Name the blood parasite species.
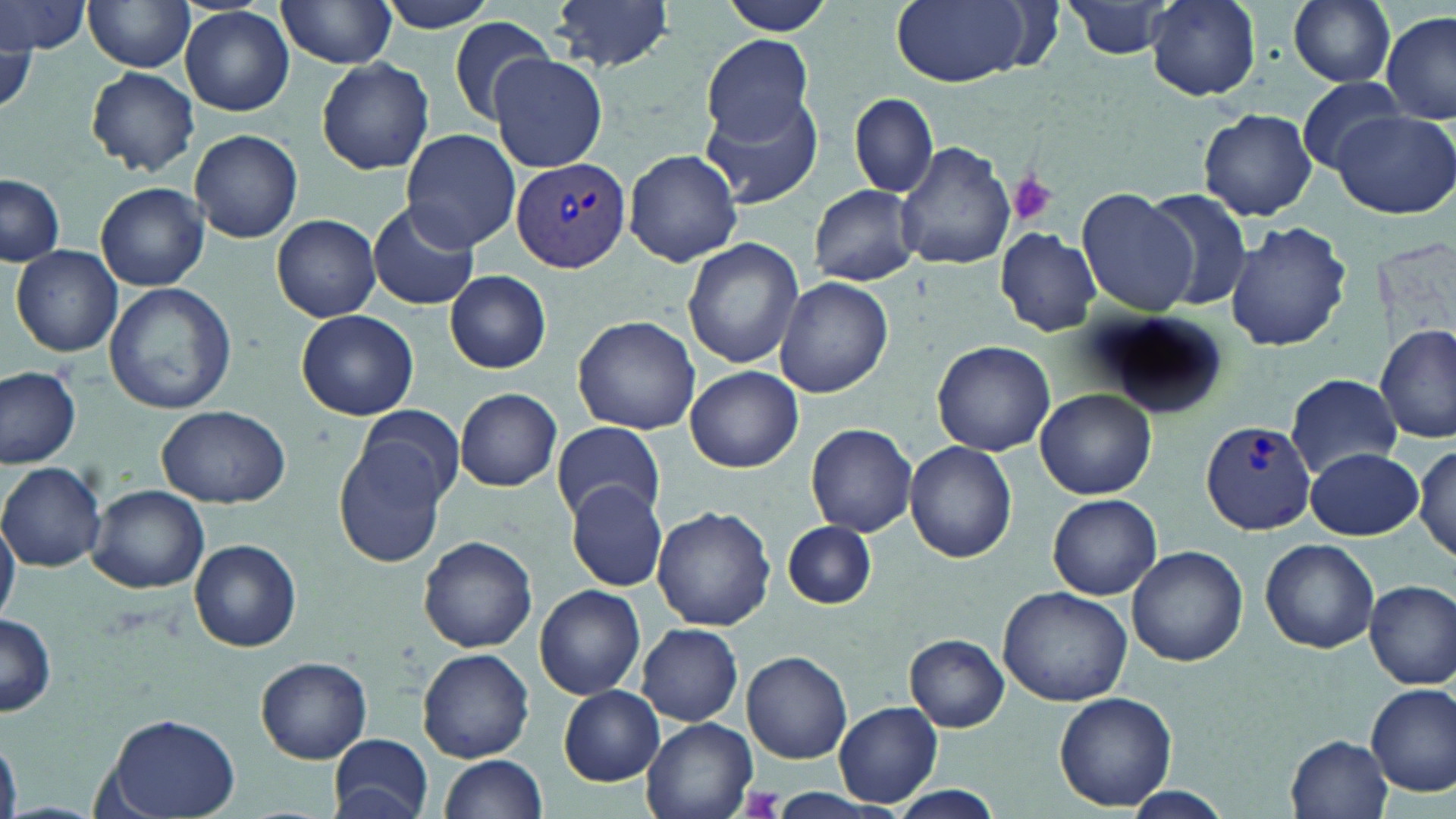

Plasmodium vivax.

Approximate bounding boxes as named x1/y1/x2/y2 corners in pixels. Platelet locations: (x1=1005, y1=171, x2=1059, y2=226), (x1=742, y1=786, x2=783, y2=817). Plasmodium vivax-infected red blood cell locations: (x1=509, y1=153, x2=632, y2=275), (x1=1200, y1=419, x2=1319, y2=534). Uninfected red blood cell locations: (x1=83, y1=0, x2=196, y2=72), (x1=275, y1=0, x2=400, y2=69), (x1=371, y1=0, x2=505, y2=33), (x1=550, y1=0, x2=674, y2=74), (x1=720, y1=0, x2=834, y2=36), (x1=889, y1=0, x2=1039, y2=87), (x1=1061, y1=0, x2=1180, y2=59), (x1=1145, y1=0, x2=1260, y2=101), (x1=1287, y1=0, x2=1397, y2=87), (x1=0, y1=2, x2=90, y2=57), (x1=181, y1=5, x2=295, y2=116), (x1=1382, y1=12, x2=1456, y2=125), (x1=446, y1=16, x2=555, y2=125), (x1=0, y1=31, x2=34, y2=118), (x1=701, y1=35, x2=816, y2=143), (x1=489, y1=53, x2=609, y2=172), (x1=316, y1=59, x2=435, y2=174), (x1=85, y1=66, x2=199, y2=176), (x1=1296, y1=78, x2=1411, y2=172), (x1=850, y1=93, x2=937, y2=198), (x1=702, y1=96, x2=823, y2=208), (x1=1199, y1=108, x2=1317, y2=220), (x1=1331, y1=109, x2=1456, y2=219), (x1=189, y1=129, x2=303, y2=243), (x1=402, y1=130, x2=520, y2=251), (x1=896, y1=141, x2=1015, y2=270), (x1=623, y1=148, x2=743, y2=267), (x1=0, y1=173, x2=64, y2=266), (x1=96, y1=183, x2=210, y2=291), (x1=810, y1=185, x2=919, y2=286), (x1=1077, y1=187, x2=1198, y2=316), (x1=1138, y1=187, x2=1252, y2=313), (x1=367, y1=203, x2=480, y2=310), (x1=272, y1=214, x2=382, y2=322), (x1=1225, y1=220, x2=1351, y2=352), (x1=995, y1=227, x2=1101, y2=336), (x1=683, y1=238, x2=805, y2=369), (x1=11, y1=245, x2=123, y2=356), (x1=445, y1=270, x2=551, y2=374), (x1=774, y1=276, x2=892, y2=398), (x1=104, y1=280, x2=237, y2=415), (x1=296, y1=309, x2=419, y2=421), (x1=1090, y1=310, x2=1226, y2=419), (x1=573, y1=315, x2=700, y2=433), (x1=1376, y1=323, x2=1455, y2=443), (x1=933, y1=340, x2=1055, y2=456), (x1=685, y1=364, x2=802, y2=472), (x1=0, y1=365, x2=81, y2=469), (x1=1286, y1=372, x2=1404, y2=478), (x1=455, y1=387, x2=561, y2=491), (x1=1036, y1=390, x2=1157, y2=499), (x1=156, y1=405, x2=290, y2=507), (x1=351, y1=405, x2=467, y2=508), (x1=552, y1=420, x2=665, y2=524), (x1=805, y1=423, x2=918, y2=538), (x1=335, y1=440, x2=450, y2=567), (x1=904, y1=441, x2=1017, y2=563), (x1=1411, y1=443, x2=1454, y2=563), (x1=1305, y1=447, x2=1424, y2=540), (x1=1, y1=463, x2=106, y2=571), (x1=566, y1=482, x2=668, y2=591), (x1=87, y1=485, x2=210, y2=595), (x1=1048, y1=494, x2=1162, y2=600), (x1=653, y1=505, x2=776, y2=631), (x1=0, y1=510, x2=20, y2=627), (x1=780, y1=520, x2=880, y2=612), (x1=418, y1=535, x2=538, y2=653), (x1=1260, y1=538, x2=1380, y2=652), (x1=189, y1=539, x2=301, y2=652), (x1=1127, y1=545, x2=1248, y2=666), (x1=1365, y1=579, x2=1455, y2=689), (x1=534, y1=584, x2=644, y2=700), (x1=998, y1=585, x2=1133, y2=707), (x1=0, y1=614, x2=58, y2=717), (x1=637, y1=623, x2=743, y2=726), (x1=907, y1=635, x2=1010, y2=732), (x1=417, y1=647, x2=535, y2=762), (x1=741, y1=651, x2=853, y2=764), (x1=257, y1=656, x2=373, y2=763), (x1=1366, y1=680, x2=1456, y2=798), (x1=558, y1=686, x2=663, y2=786), (x1=1055, y1=691, x2=1177, y2=810), (x1=834, y1=701, x2=943, y2=807), (x1=102, y1=712, x2=242, y2=819), (x1=641, y1=716, x2=758, y2=819), (x1=329, y1=733, x2=433, y2=818), (x1=1286, y1=734, x2=1393, y2=818), (x1=0, y1=739, x2=22, y2=819), (x1=439, y1=754, x2=548, y2=819), (x1=879, y1=786, x2=1006, y2=819), (x1=1115, y1=787, x2=1237, y2=817). Thin blood smear. Image is 1456×819 pixels. May-Grünwald-Giemsa-stained preparation. Light microscopy. One field of a larger specimen. 1000x magnification.